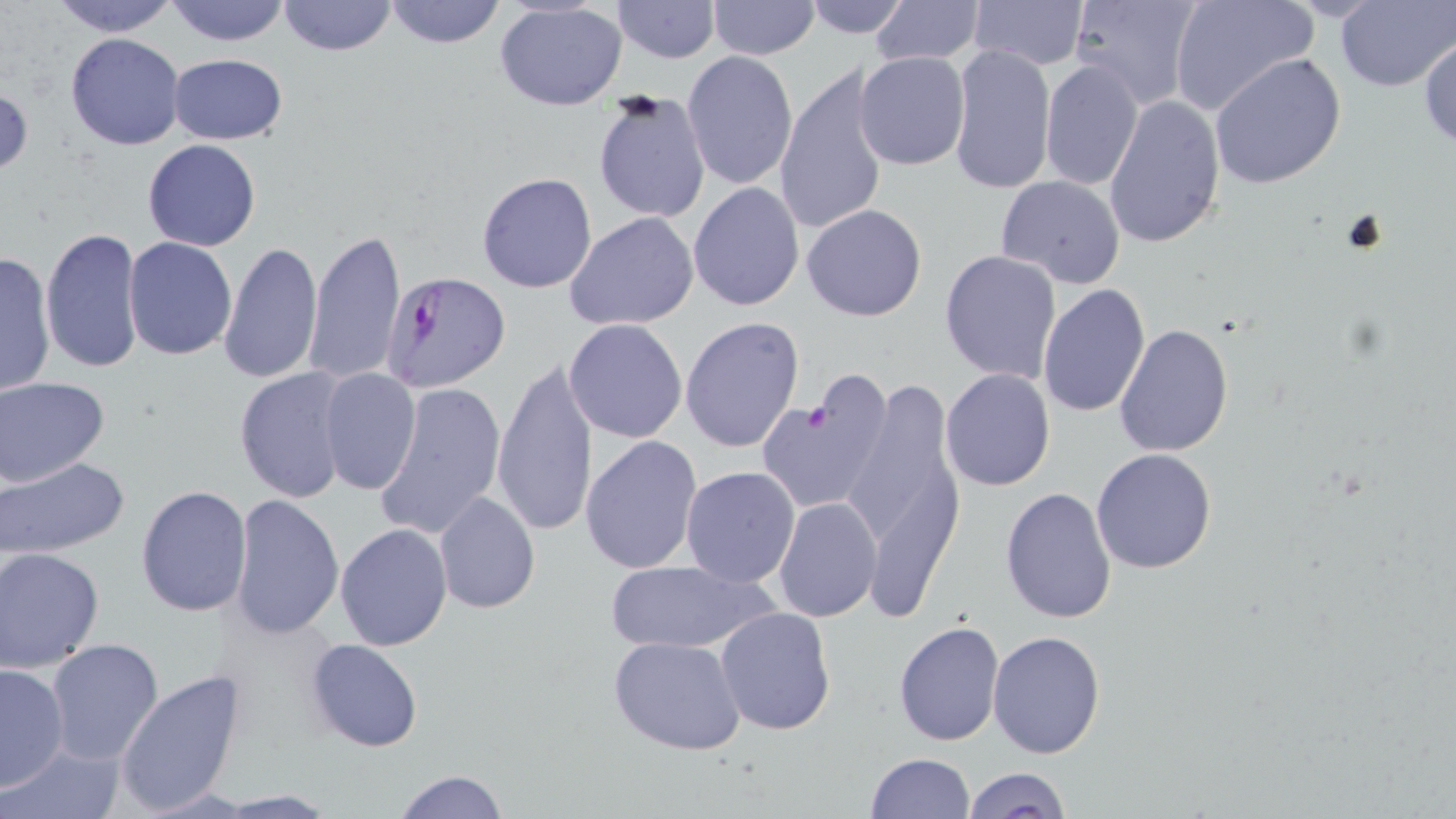 Approximate bounding boxes as [x1, y1, x2, y2] in pixels. Platelet locations: [802, 400, 837, 434]. Plasmodium falciparum-infected red blood cell locations: [382, 271, 512, 393]. Uninfected red blood cell locations: [46, 0, 183, 37], [164, 0, 290, 47], [277, 0, 396, 57], [383, 0, 507, 49], [707, 0, 820, 59], [802, 0, 912, 39], [868, 0, 985, 66], [970, 0, 1088, 71], [1067, 0, 1205, 109], [1168, 0, 1317, 116], [611, 1, 719, 63], [1335, 1, 1456, 92], [496, 2, 627, 111], [65, 33, 185, 150], [1418, 33, 1456, 151], [948, 44, 1055, 195], [681, 51, 799, 191], [855, 52, 971, 171], [1210, 52, 1346, 190], [168, 54, 288, 144], [1039, 58, 1142, 192], [774, 63, 890, 239], [0, 82, 33, 181], [591, 92, 711, 222], [1101, 93, 1227, 250], [142, 139, 261, 251], [478, 172, 598, 293], [995, 175, 1127, 289], [688, 182, 805, 312], [801, 203, 928, 322], [565, 211, 698, 331], [41, 226, 144, 374], [303, 228, 406, 387], [123, 235, 237, 361], [218, 241, 324, 384], [939, 249, 1062, 384], [0, 250, 56, 399], [1036, 282, 1151, 417], [681, 316, 804, 453], [564, 318, 689, 442], [1113, 322, 1234, 456], [490, 356, 598, 539], [232, 367, 354, 506], [939, 368, 1056, 491], [319, 369, 420, 495], [836, 373, 969, 604], [1, 375, 110, 488], [373, 380, 506, 540], [763, 383, 891, 511], [580, 436, 704, 575], [1092, 448, 1217, 574], [1, 455, 131, 559], [680, 466, 800, 587], [135, 485, 253, 616], [1000, 486, 1118, 625], [433, 492, 540, 613], [228, 493, 342, 639], [774, 496, 881, 623], [335, 522, 452, 650], [0, 546, 104, 673], [604, 558, 778, 656], [715, 605, 836, 735], [892, 619, 1005, 746], [988, 629, 1106, 759], [608, 637, 748, 754], [46, 638, 164, 765], [304, 639, 424, 753], [0, 663, 70, 789], [114, 669, 246, 814], [2, 740, 126, 819], [865, 752, 977, 818], [963, 766, 1071, 819], [392, 770, 508, 819], [208, 790, 340, 816]. Slide-level diagnosis: Plasmodium falciparum. 1000x magnification. Single field of view. Optical microscopy. Thin blood film. May-Grünwald-Giemsa-stained preparation. Image is 1456×819 pixels.